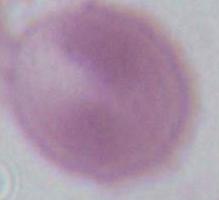

magnification = 1000x
identification = erythrocyte
modality = photomicrograph